Outline each blood parasite and name the species.
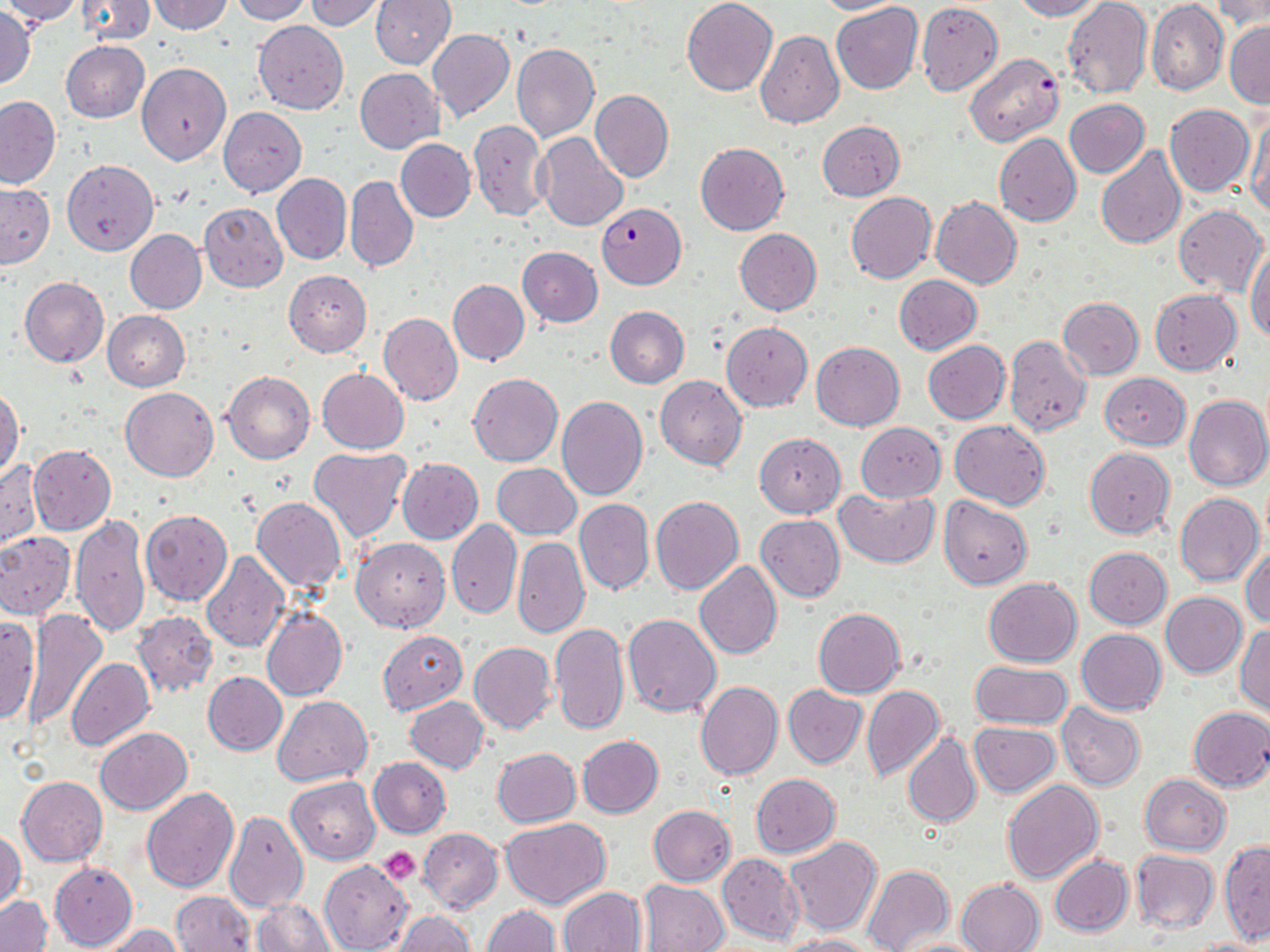

Approximate bounding boxes as (x1, y1, x2, y2) in pixels.
Plasmodium falciparum-infected red blood cells: (963, 52, 1064, 147), (596, 203, 686, 288).
No Plasmodium ovale, Plasmodium malariae, Plasmodium vivax, Babesia divergens, or Trypanosoma brucei observed.

{
  "slide_level_diagnosis": "Plasmodium falciparum",
  "stain": "May-Grünwald-Giemsa",
  "modality": "light microscopy",
  "preparation": "thin blood smear",
  "platelet_locations": "approximate bounding boxes as (x1, y1, x2, y2) in pixels: (379, 847, 421, 885)",
  "uninfected_red_blood_cell_locations": "approximate bounding boxes as (x1, y1, x2, y2) in pixels: (0, 0, 84, 25), (74, 0, 154, 45), (151, 0, 232, 34), (231, 0, 313, 23), (370, 0, 455, 69), (681, 0, 778, 96), (812, 0, 914, 15), (1008, 0, 1101, 20), (1147, 0, 1227, 95), (307, 1, 387, 31), (831, 1, 923, 95), (1063, 1, 1152, 101), (1213, 2, 1270, 33), (916, 3, 1003, 96), (0, 7, 36, 89), (252, 20, 348, 113), (1224, 21, 1269, 108), (427, 28, 514, 123), (756, 30, 843, 128), (62, 41, 149, 123), (511, 44, 599, 143), (137, 63, 232, 166), (354, 69, 444, 152), (590, 89, 673, 183), (0, 96, 60, 189), (1064, 99, 1150, 177), (1165, 104, 1255, 196), (218, 107, 306, 197), (1244, 112, 1270, 217), (468, 119, 549, 222), (817, 120, 904, 201), (535, 133, 629, 231), (993, 133, 1081, 227), (395, 139, 476, 222), (695, 142, 788, 234), (1094, 146, 1185, 248), (63, 159, 158, 255), (272, 173, 351, 265), (345, 176, 417, 272), (0, 184, 54, 268), (844, 192, 936, 283), (931, 197, 1022, 290), (199, 202, 288, 292), (1173, 205, 1268, 296), (734, 228, 822, 315), (125, 230, 206, 314), (517, 246, 603, 327), (1246, 250, 1270, 343), (283, 270, 371, 357), (894, 275, 983, 355), (20, 277, 108, 367), (448, 279, 529, 365), (1149, 288, 1240, 375), (1057, 296, 1143, 379), (605, 305, 689, 388), (103, 311, 190, 391), (379, 313, 463, 405), (721, 322, 812, 411), (1003, 336, 1092, 436), (922, 339, 1009, 424), (811, 341, 904, 431), (316, 368, 409, 453), (221, 370, 315, 463), (467, 372, 563, 467), (1100, 372, 1189, 449), (656, 376, 747, 470), (0, 387, 23, 477), (121, 387, 218, 480), (1184, 394, 1270, 491), (556, 395, 647, 499), (949, 419, 1050, 510), (855, 422, 946, 500), (755, 433, 845, 518), (29, 445, 116, 535), (1084, 447, 1174, 538), (308, 448, 410, 542), (1, 458, 42, 549), (396, 458, 483, 544), (491, 463, 581, 540), (833, 487, 938, 567), (1175, 493, 1263, 585), (651, 494, 744, 595), (251, 496, 346, 591), (939, 497, 1032, 589), (575, 498, 653, 594), (141, 511, 232, 605), (70, 514, 150, 637), (756, 515, 844, 602), (447, 519, 521, 618), (0, 532, 75, 620), (353, 537, 450, 631), (512, 537, 588, 638), (1242, 544, 1270, 629), (1084, 547, 1171, 628), (200, 550, 288, 652), (694, 562, 782, 658), (658, 565, 773, 715), (983, 577, 1082, 666), (1161, 592, 1246, 677), (261, 605, 348, 702), (814, 607, 905, 698), (22, 608, 106, 728), (132, 611, 217, 698), (623, 613, 721, 715), (0, 615, 40, 726), (550, 623, 629, 735), (1235, 625, 1270, 716), (1077, 629, 1166, 714), (377, 630, 467, 714), (469, 642, 557, 734), (66, 657, 155, 749), (970, 660, 1072, 727), (203, 671, 287, 755), (695, 682, 782, 782), (783, 685, 867, 768), (861, 685, 944, 782), (272, 695, 372, 786), (406, 697, 489, 773), (1056, 703, 1145, 790), (1187, 706, 1270, 791), (969, 722, 1060, 796), (94, 727, 192, 814), (903, 732, 982, 829), (577, 735, 663, 818), (491, 748, 580, 827), (368, 758, 450, 838), (751, 773, 840, 857), (1140, 774, 1230, 854), (17, 776, 107, 866), (286, 776, 380, 864), (1002, 779, 1103, 883), (143, 788, 239, 892), (648, 805, 736, 886), (223, 810, 308, 912), (501, 818, 611, 908), (1, 828, 24, 911), (418, 828, 503, 913), (784, 836, 882, 935), (1218, 841, 1270, 944), (1131, 850, 1218, 934), (717, 853, 804, 945), (1049, 854, 1133, 937), (319, 859, 411, 951), (49, 862, 137, 949), (862, 863, 954, 952), (956, 878, 1046, 952), (637, 879, 731, 952), (558, 886, 646, 951), (169, 890, 256, 952), (1, 895, 51, 952), (253, 899, 335, 951), (481, 905, 560, 952), (391, 911, 474, 952), (101, 925, 181, 952), (778, 935, 878, 952), (1184, 937, 1268, 952), (894, 938, 993, 952)",
  "image_size": "1270×952 pixels",
  "field_of_view": "one of a larger specimen",
  "magnification": "1000x"
}